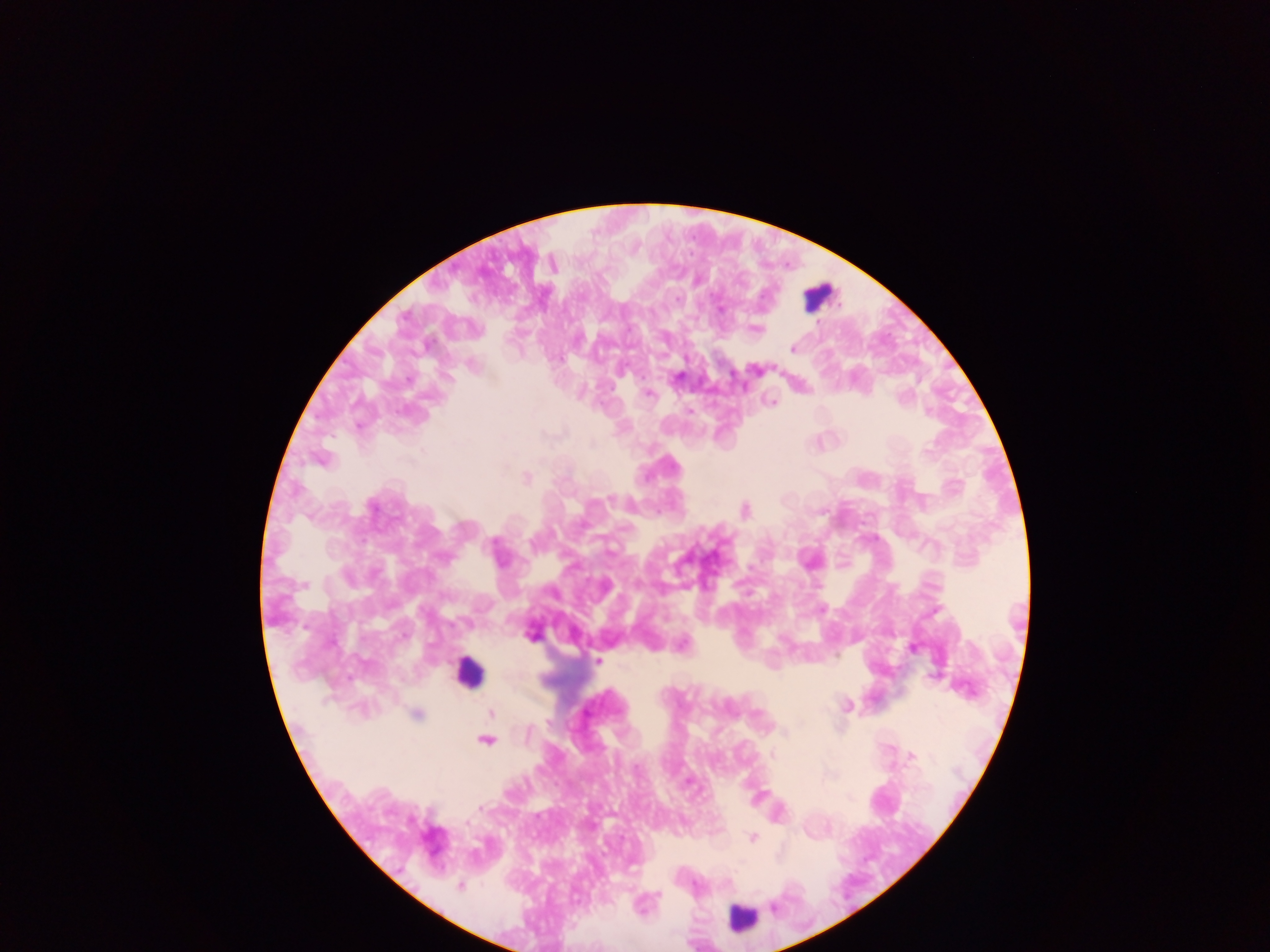

Approximate centers as {x, y} in pixels.
Summary:
  - Leukocyte locations: {819, 295}, {469, 673}, {742, 916}
  - Plasmodium parasite locations: {677, 299}, {721, 309}, {756, 329}, {793, 349}, {756, 370}, {678, 376}, {407, 380}, {648, 394}, {902, 397}, {770, 401}, {690, 411}, {592, 444}, {927, 451}, {527, 478}, {611, 499}, {373, 506}, {745, 511}, {531, 542}, {445, 558}, {822, 609}, {530, 636}, {683, 644}, {913, 648}, {598, 661}, {846, 705}, {491, 713}, {416, 715}, {548, 721}, {784, 732}, {528, 733}, {486, 740}, {911, 755}, {772, 756}, {637, 768}, {687, 782}, {480, 807}, {466, 822}, {752, 838}, {460, 886}, {774, 908}
  - Field of view: single
  - Preparation: thick blood film
  - Capture: mobile-phone photograph through a microscope
  - Country: Ghana
  - Image size: 1270×952 pixels